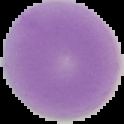
Malaria status: uninfected. From a thin blood smear. The area outside the segmented cell region is set to black. Image is 124×124 pixels.